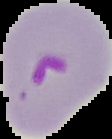
Summary:
  - Preparation: thin blood film
  - Result: Plasmodium parasites detected
  - Image size: 112×139 pixels
  - Image type: segmented cell region with the area outside set to black